Classify this cell by malaria status.
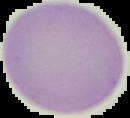
Uninfected.

From a thin blood smear. Image is 130×118 pixels. Segmented cell region on a black background.